Name the parasite shown.
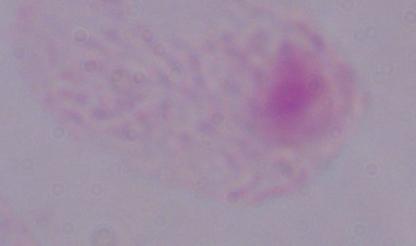

A trichomonad.

modality = micrograph
magnification = 1000x